State which parasite is depicted.
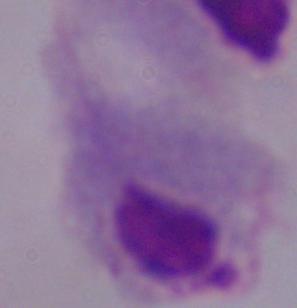

This is a trichomonad.

Summary:
  - Modality: micrograph
  - Magnification: 1000x